Identify the cell.
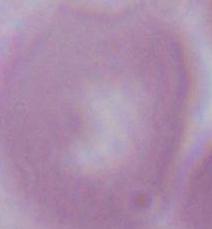

This is an erythrocyte.

Captured at 1000x magnification. Photomicrograph.